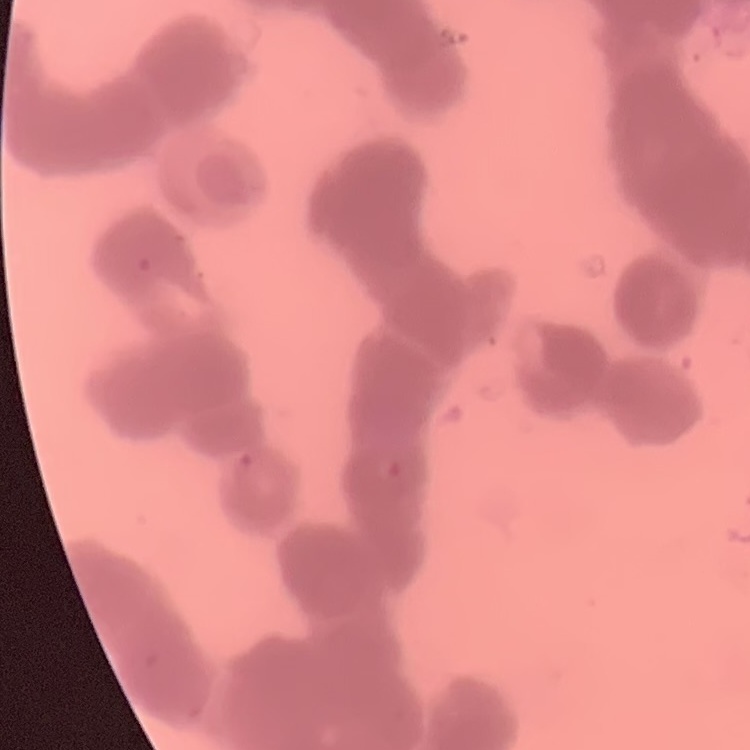
red blood cell morphology = rouleaux formation
preparation = thin peripheral smear
stain = Field's or Giemsa
image type = square crop of a larger photomicrograph